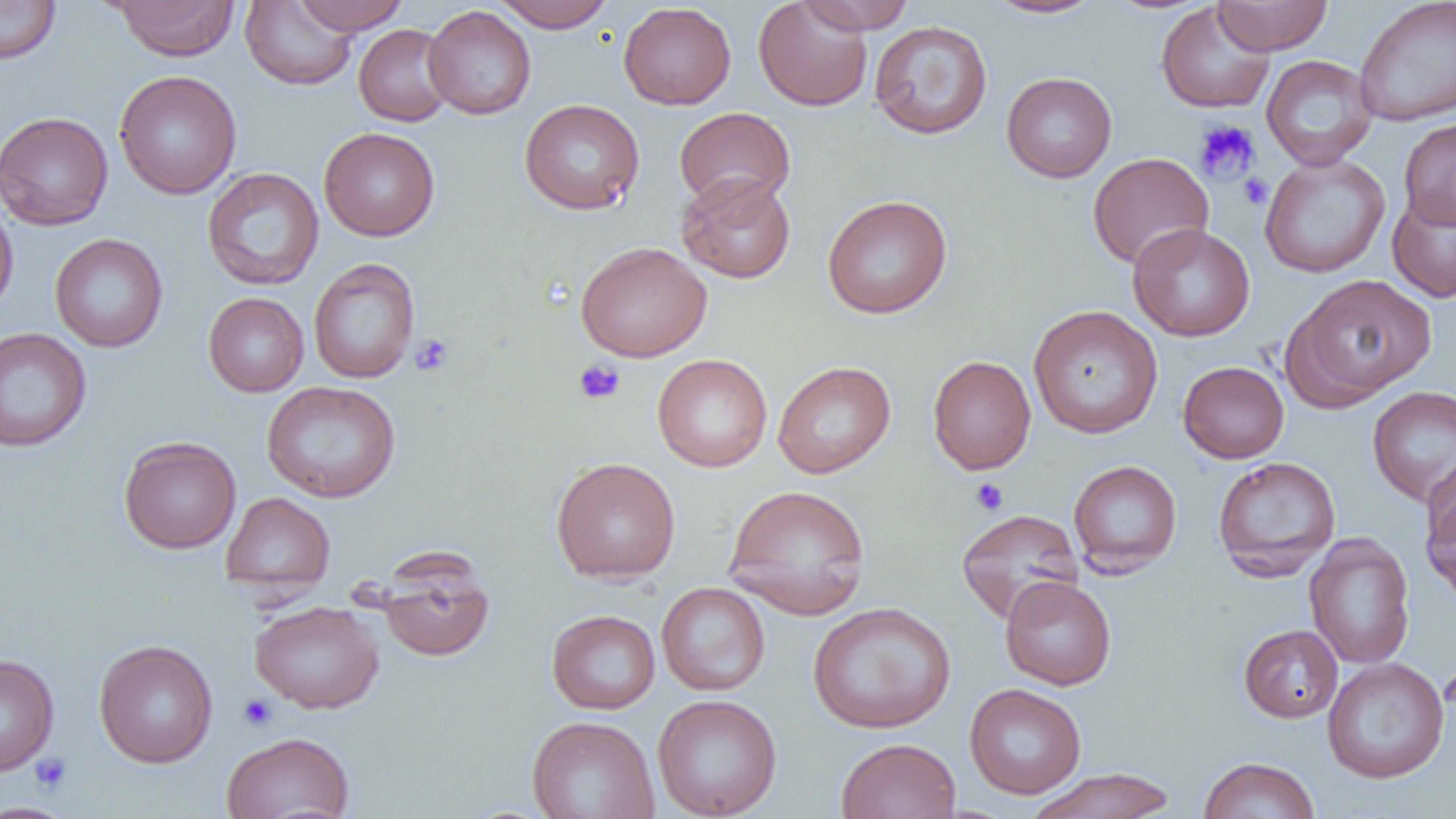

Approximate bounding boxes as (x1,y1)-(x2,y2) corner pairs in pixels. Platelet locations: (1193,119)-(1261,185), (1238,173)-(1272,210), (410,334)-(454,376), (573,359)-(625,405), (970,478)-(1009,516), (238,694)-(278,730), (30,751)-(72,793). Uninfected red blood cell locations: (0,0)-(62,65), (291,0)-(409,35), (491,0)-(615,31), (753,0)-(874,112), (796,0)-(916,34), (985,0)-(1104,19), (1211,0)-(1332,55), (1354,0)-(1456,126), (109,1)-(241,61), (240,1)-(358,90), (618,2)-(736,109), (1155,3)-(1275,114), (423,5)-(536,120), (869,20)-(993,140), (353,24)-(455,127), (1261,54)-(1378,171), (113,70)-(242,199), (1001,72)-(1117,182), (519,98)-(645,215), (674,107)-(795,210), (0,111)-(114,231), (1399,118)-(1456,229), (318,127)-(440,241), (1087,152)-(1214,270), (1260,153)-(1391,278), (202,167)-(324,290), (676,172)-(796,283), (1386,187)-(1456,303), (822,195)-(953,318), (0,197)-(19,321), (1127,222)-(1255,342), (50,233)-(168,352), (575,241)-(712,361), (308,257)-(420,384), (1284,273)-(1438,407), (203,292)-(309,397), (1028,305)-(1163,439), (0,327)-(92,452), (652,353)-(772,472), (927,355)-(1036,474), (772,361)-(896,479), (1177,361)-(1289,463), (261,380)-(401,503), (1367,385)-(1456,508), (118,436)-(242,553), (1421,454)-(1456,556), (551,456)-(681,583), (1212,456)-(1341,580), (1068,459)-(1182,576), (723,483)-(871,618), (221,491)-(335,596), (1421,491)-(1456,604), (956,509)-(1083,624), (1303,532)-(1415,670), (375,559)-(494,662), (1000,575)-(1116,690), (657,582)-(770,696), (249,601)-(385,714), (807,602)-(956,733), (546,609)-(661,714), (1238,624)-(1343,722), (93,639)-(218,768), (0,653)-(60,775), (1322,657)-(1449,784), (964,683)-(1086,799), (652,694)-(782,819), (527,715)-(659,819), (221,731)-(355,819), (836,737)-(962,819), (1198,756)-(1321,818), (1024,767)-(1178,819), (0,801)-(78,818). Slide-level diagnosis: negative for blood parasites. Thin blood smear. Image is 1456×819 pixels. Captured at 1000x magnification. Single field of view. Optical microscopy.